Name the blood parasite species.
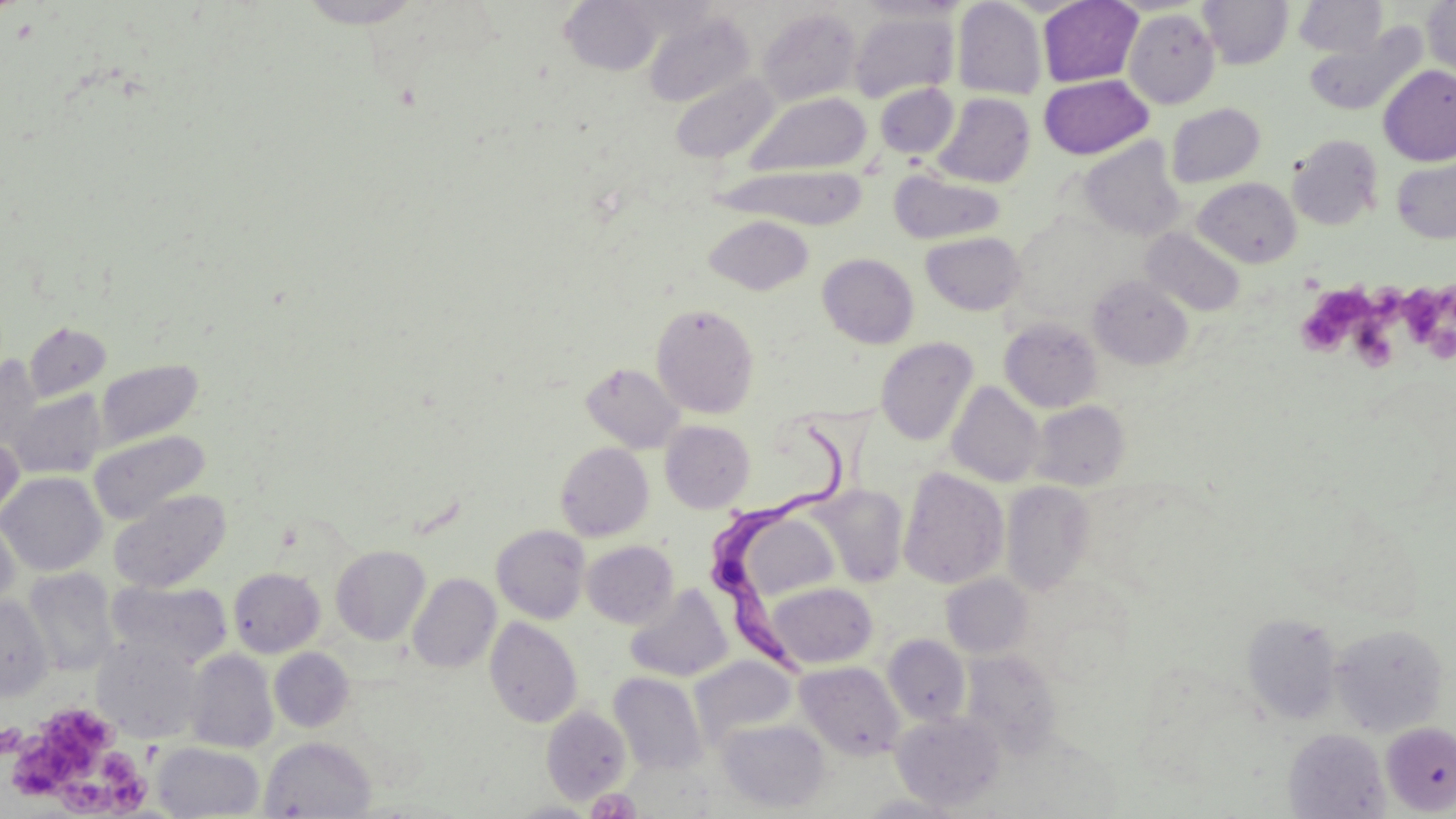
Trypanosoma brucei.

Approximate bounding boxes as (x1, y1, x2, y2) in pixels. Uninfected red blood cell locations: (559, 0, 665, 75), (952, 0, 1048, 100), (1037, 0, 1143, 87), (1198, 0, 1293, 69), (1292, 0, 1388, 58), (1422, 0, 1456, 80), (293, 1, 431, 29), (857, 1, 970, 23), (757, 7, 862, 107), (849, 9, 959, 102), (1123, 9, 1220, 108), (643, 10, 755, 108), (1303, 24, 1427, 117), (1378, 65, 1456, 166), (669, 72, 779, 163), (1038, 74, 1153, 160), (875, 83, 958, 158), (744, 91, 871, 178), (933, 93, 1035, 188), (1166, 103, 1265, 188), (1287, 134, 1384, 230), (1079, 138, 1185, 241), (1392, 158, 1456, 243), (715, 164, 866, 229), (890, 169, 1006, 245), (1193, 177, 1301, 267), (703, 214, 814, 295), (1141, 227, 1245, 317), (921, 231, 1026, 315), (818, 253, 919, 349), (1087, 274, 1194, 370), (651, 303, 760, 418), (999, 317, 1103, 412), (23, 322, 111, 402), (874, 337, 979, 446), (0, 357, 45, 455), (93, 358, 204, 449), (581, 361, 685, 453), (946, 382, 1045, 487), (7, 389, 106, 479), (1028, 400, 1131, 491), (660, 420, 755, 513), (89, 430, 211, 524), (0, 432, 24, 529), (555, 442, 654, 541), (898, 467, 1009, 589), (0, 472, 106, 576), (1001, 481, 1096, 595), (814, 485, 910, 587), (109, 489, 231, 592), (733, 510, 840, 602), (0, 513, 20, 615), (492, 525, 590, 624), (582, 540, 678, 628), (331, 545, 430, 645), (227, 563, 430, 653), (22, 567, 120, 676), (228, 567, 325, 657), (408, 573, 501, 673), (941, 573, 1034, 658), (107, 579, 233, 670), (766, 581, 877, 669), (625, 583, 733, 683), (0, 595, 53, 700), (1242, 613, 1342, 724), (485, 617, 583, 728), (1330, 622, 1449, 736), (883, 634, 971, 726), (92, 638, 204, 743), (269, 648, 355, 732), (184, 649, 278, 753), (960, 649, 1062, 756), (690, 655, 798, 750), (796, 661, 905, 760), (609, 672, 707, 775), (541, 705, 632, 804), (891, 711, 1005, 811), (716, 718, 830, 813), (1381, 721, 1456, 815), (1283, 728, 1390, 818), (259, 736, 377, 818), (152, 742, 264, 818). Trypanosoma brucei locations: (706, 418, 842, 682). Platelet locations: (1398, 285, 1450, 349), (1296, 292, 1361, 357), (1349, 323, 1400, 372), (9, 712, 142, 816), (0, 721, 23, 760). Image is 1456×819 pixels. May-Grünwald-Giemsa stain. Optical microscopy. Captured at 1000x magnification. One field of a larger specimen. Thin blood smear.